Assess this cell for malaria.
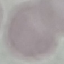

It is uninfected.

Acquired by smartphone through the microscope eyepiece. Cell patch, automatically extracted from a larger field of view and resized to 64 × 64 pixels. Thin blood film. Giemsa-stained preparation.